Name the blood parasite species.
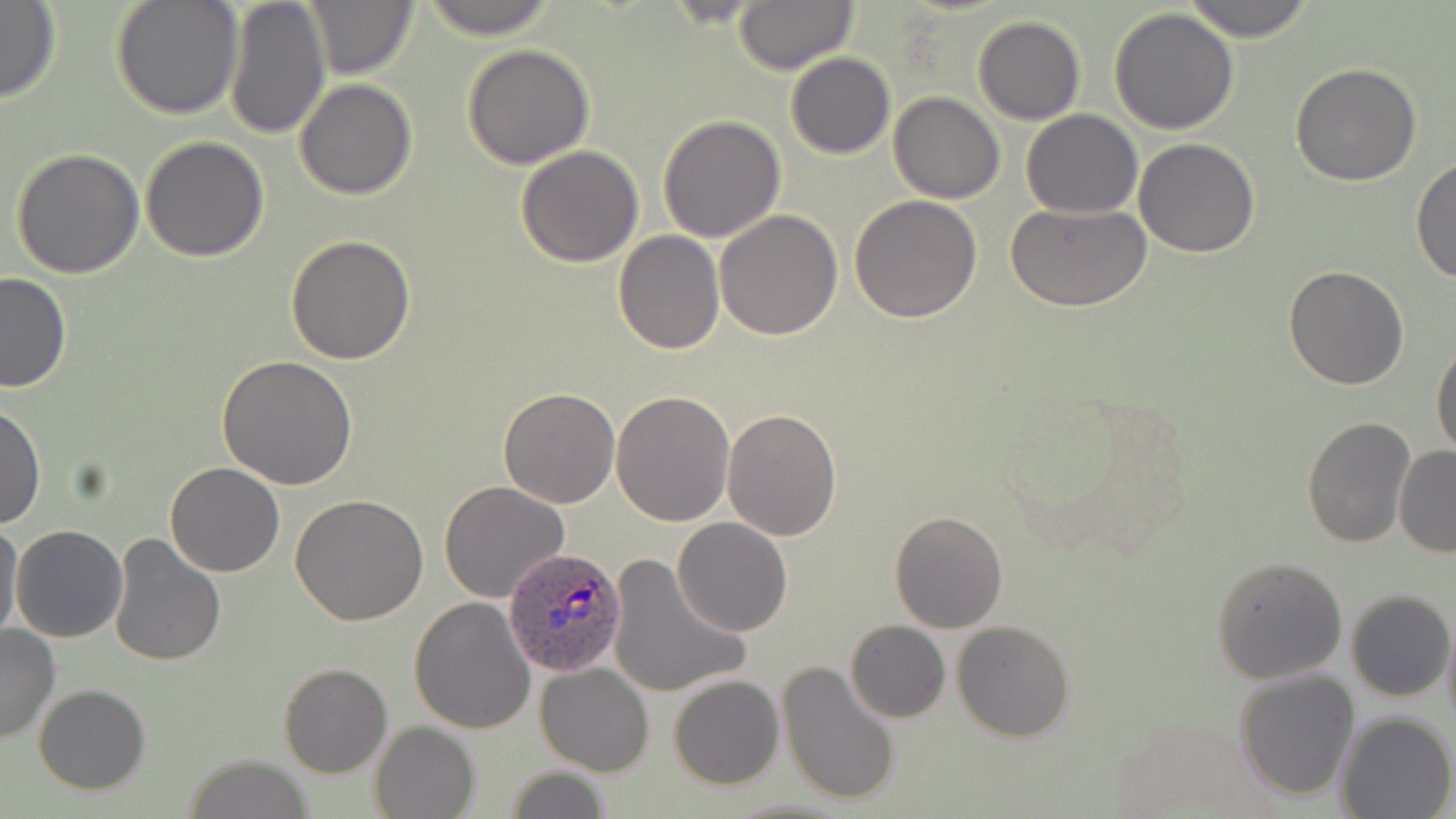
Plasmodium ovale.

Summary:
  - Coordinate format: approximate bounding boxes as (x1, y1, x2, y2) in pixels
  - Uninfected red blood cell locations: (111, 0, 244, 120), (225, 0, 330, 142), (300, 0, 419, 82), (416, 0, 563, 40), (730, 0, 858, 74), (1178, 0, 1320, 42), (0, 2, 61, 103), (1108, 7, 1240, 135), (973, 15, 1085, 124), (462, 44, 595, 170), (785, 52, 895, 159), (1290, 63, 1423, 186), (296, 79, 417, 200), (889, 92, 1005, 203), (1022, 109, 1143, 218), (658, 115, 787, 242), (140, 135, 270, 261), (1133, 138, 1261, 257), (514, 145, 644, 266), (10, 147, 145, 280), (1413, 158, 1456, 285), (849, 194, 983, 322), (1008, 203, 1151, 312), (715, 209, 842, 340), (612, 230, 724, 354), (284, 234, 415, 363), (1283, 265, 1409, 391), (0, 271, 71, 392), (1431, 343, 1456, 458), (216, 354, 357, 490), (497, 387, 621, 509), (611, 389, 736, 526), (0, 402, 45, 531), (721, 409, 843, 541), (1300, 416, 1415, 549), (1394, 447, 1456, 557), (166, 463, 284, 578), (440, 481, 570, 603), (290, 495, 428, 626), (889, 510, 1008, 632), (0, 519, 24, 644), (673, 519, 792, 637), (10, 525, 127, 643), (107, 531, 228, 667), (606, 553, 751, 700), (1213, 556, 1348, 684), (1347, 589, 1454, 702), (409, 598, 536, 734), (1441, 616, 1456, 738), (954, 619, 1074, 739), (845, 621, 950, 722), (0, 624, 60, 743), (776, 659, 902, 808), (279, 663, 392, 777), (534, 664, 654, 776), (1234, 670, 1360, 800), (669, 676, 783, 789), (33, 683, 151, 794), (1335, 713, 1454, 819), (370, 722, 479, 819), (182, 754, 319, 818), (503, 764, 613, 819)
  - Plasmodium ovale-infected red blood cell locations: (502, 546, 628, 677)
  - Modality: light microscopy
  - Preparation: thin blood smear
  - Image size: 1456×819 pixels
  - Stain: May-Grünwald-Giemsa
  - Magnification: 1000x
  - Field of view: one of a larger specimen